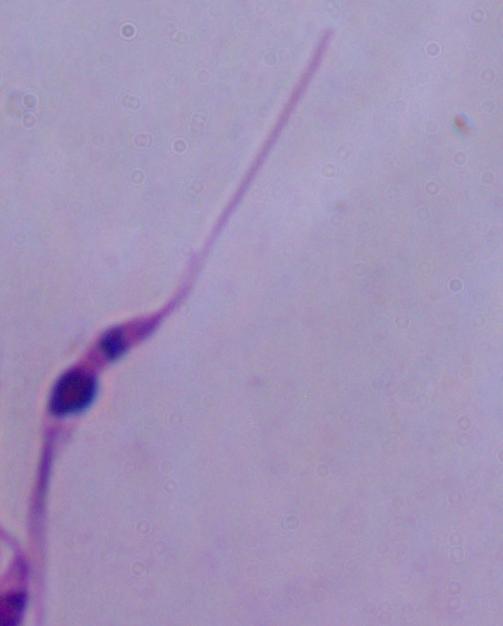
magnification = 1000x
modality = photomicrograph
identification = Leishmania